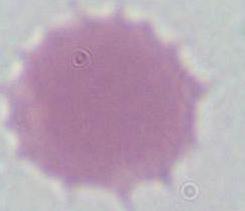

identification = erythrocyte
magnification = 1000x
modality = micrograph